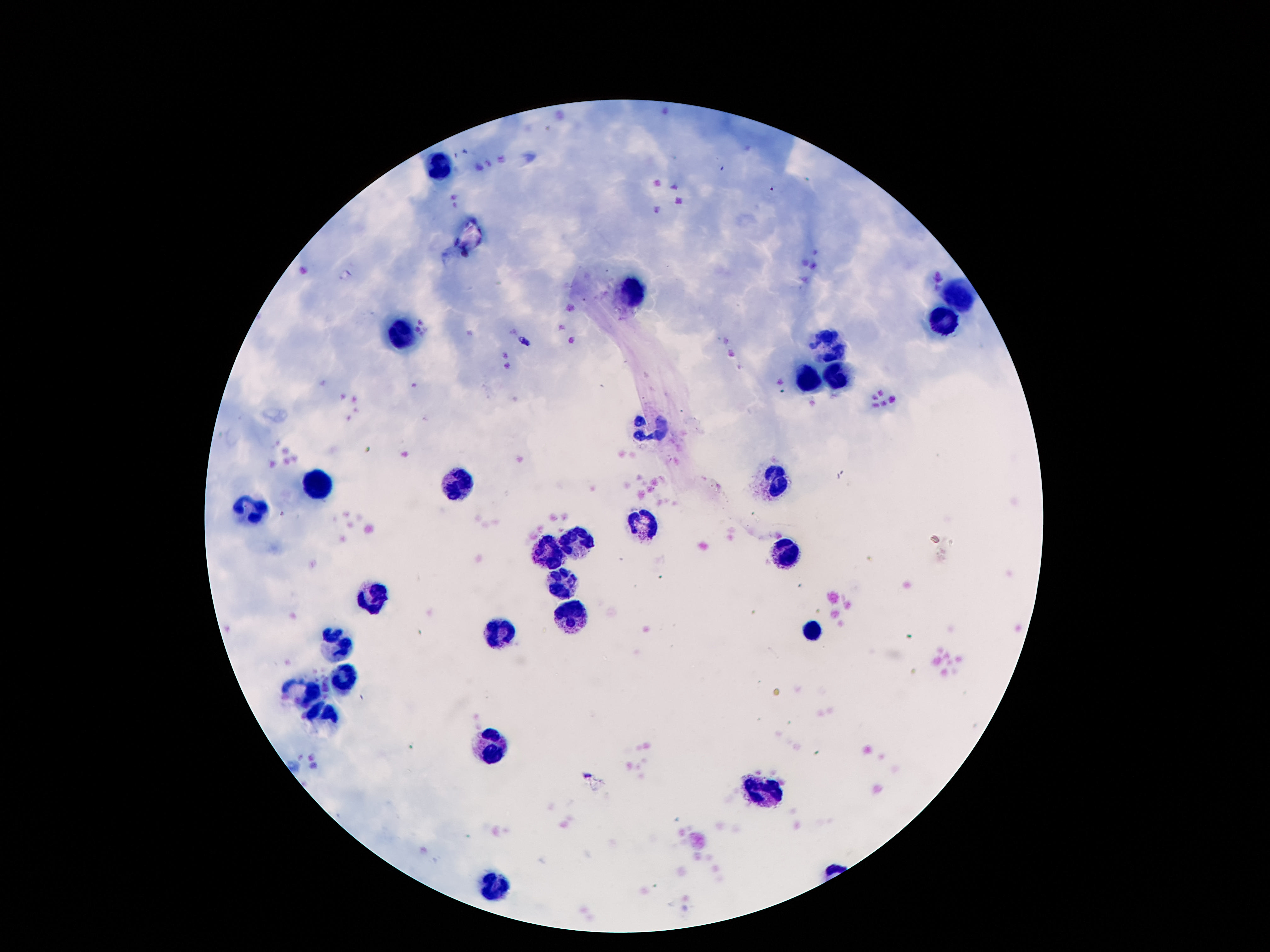

preparation: thick blood film
leukocyte_locations: 'approximate centers as (x, y) in pixels: (443, 163), (633, 294), (953, 298), (947, 325), (403, 334), (832, 342), (834, 377), (808, 379), (651, 424), (317, 479), (777, 482), (456, 484), (251, 506), (642, 524), (580, 544), (551, 550), (788, 555), (560, 581), (374, 592), (573, 609), (503, 630), (814, 631), (339, 643), (346, 676), (304, 696), (326, 714), (487, 745), (761, 790), (494, 886)'
field_of_view: one from this slide
image_size: 1270×952 pixels
magnification: 100x
capture: smartphone camera through the microscope eyepiece
stain: Giemsa
patient_malaria_status: uninfected